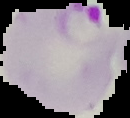

image_type: segmented cell region with the area outside set to black
malaria_status: parasitized
preparation: thin blood smear
image_size: 130×118 pixels